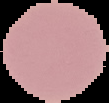 Image is 109×103 pixels. Segmented cell region on a black background. Result: negative for malaria parasites. From a thin blood smear.